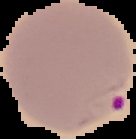 From a thin blood smear. Result: Plasmodium parasites identified. Cell region segmented out of the field of view; the surrounding area is masked to black. Image is 136×139 pixels.